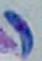
Summary:
  - Modality: micrograph
  - Magnification: 1000x
  - Identification: Toxoplasma gondii